Identify the blood parasite species.
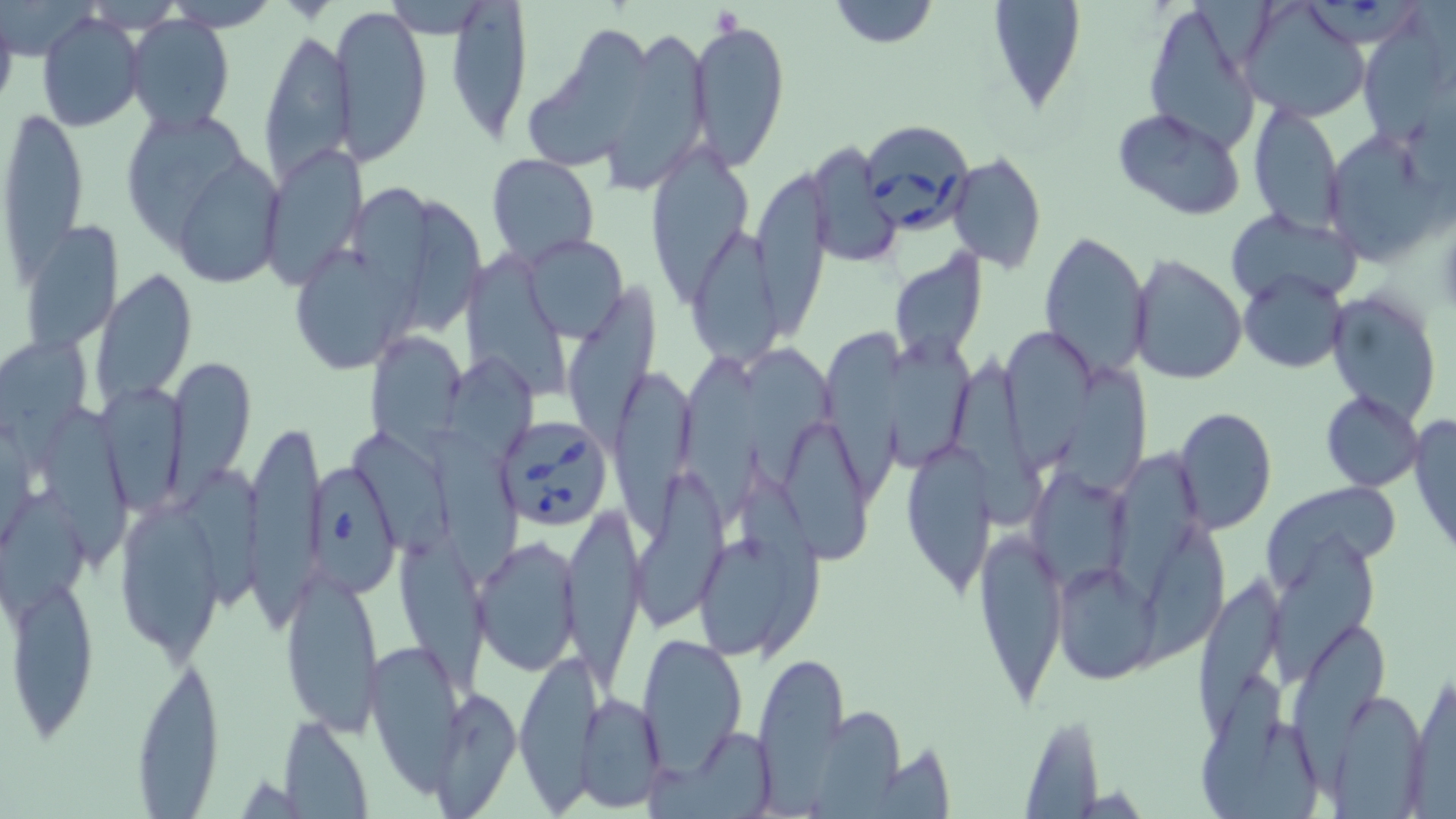

Babesia divergens.

Approximate bounding boxes as [x1, y1, x2, y2] in pixels. Uninfected red blood cell locations: [828, 0, 939, 50], [986, 0, 1085, 113], [331, 3, 432, 165], [1140, 3, 1265, 157], [1236, 3, 1371, 124], [444, 4, 532, 145], [38, 12, 146, 131], [125, 16, 235, 135], [689, 16, 791, 170], [1357, 18, 1454, 146], [521, 23, 657, 172], [258, 25, 355, 188], [599, 25, 712, 189], [1245, 102, 1345, 232], [3, 106, 90, 286], [1114, 108, 1246, 220], [130, 112, 251, 257], [1322, 129, 1445, 263], [644, 137, 755, 305], [262, 142, 368, 288], [806, 142, 900, 268], [486, 153, 600, 264], [946, 153, 1047, 271], [180, 161, 284, 283], [759, 164, 830, 342], [353, 186, 436, 299], [404, 199, 488, 340], [1226, 209, 1363, 308], [689, 219, 780, 371], [23, 221, 123, 351], [1038, 229, 1152, 379], [520, 236, 628, 338], [287, 240, 415, 375], [888, 251, 988, 365], [1129, 254, 1248, 387], [472, 258, 570, 405], [1238, 268, 1350, 375], [90, 269, 196, 417], [568, 278, 663, 458], [1327, 289, 1442, 420], [886, 328, 968, 470], [366, 330, 466, 444], [1003, 330, 1089, 468], [821, 331, 905, 502], [1, 340, 87, 470], [745, 349, 832, 478], [684, 352, 760, 521], [955, 354, 1041, 523], [168, 355, 256, 495], [446, 356, 536, 464], [608, 363, 698, 532], [1064, 364, 1146, 491], [1320, 392, 1425, 492], [102, 394, 192, 513], [1172, 405, 1277, 533], [46, 406, 134, 562], [1408, 412, 1456, 561], [245, 417, 323, 612], [772, 423, 870, 562], [425, 426, 517, 581], [354, 430, 452, 558], [903, 439, 993, 598], [1114, 443, 1197, 596], [1030, 468, 1129, 587], [184, 470, 264, 608], [736, 470, 822, 659], [637, 472, 726, 629], [1265, 483, 1399, 577], [2, 485, 89, 629], [114, 500, 225, 659], [560, 503, 645, 689], [398, 518, 489, 690], [1137, 520, 1222, 662], [973, 526, 1069, 707], [1271, 531, 1379, 690], [473, 534, 582, 676], [693, 536, 810, 661], [1053, 563, 1157, 683], [281, 567, 384, 734], [7, 568, 98, 739], [1195, 574, 1277, 744], [1291, 626, 1389, 798], [636, 633, 747, 777], [365, 639, 464, 783], [514, 647, 601, 806], [754, 648, 850, 807], [131, 653, 223, 810], [1406, 670, 1455, 815], [1200, 673, 1284, 819], [431, 686, 521, 815], [1322, 688, 1430, 814], [576, 692, 666, 812], [811, 705, 911, 814], [1017, 714, 1107, 816], [278, 715, 374, 818], [677, 727, 777, 817]. Platelet locations: [711, 8, 740, 36]. Babesia divergens-infected red blood cell locations: [859, 121, 973, 234], [494, 416, 614, 532], [308, 466, 397, 591]. May-Grünwald-Giemsa stain. Thin blood film. Image is 1456×819 pixels. Optical microscopy. Single field of view. 1000x magnification.